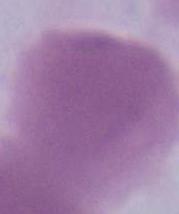

A red blood cell is shown. Micrograph. 1000x magnification.